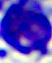

Summary:
  - Modality: photomicrograph
  - Identification: leukocyte
  - Magnification: 400x